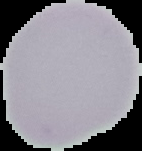

Summary:
  - Image type: cell region segmented out of the field of view; surrounding area masked to black
  - Result: no malaria parasites seen
  - Preparation: thin blood film
  - Image size: 142×151 pixels